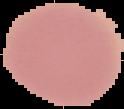
image type = cell region segmented out of the field of view; surrounding area masked to black
image size = 124×109 pixels
result = no Plasmodium parasites seen
preparation = thin blood film